Classify this cell by malaria status.
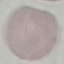

It is uninfected.

Summary:
  - Preparation: thin smear
  - Stain: Giemsa
  - Image type: cell patch, automatically extracted from a larger field of view and resized to 64 × 64 pixels
  - Capture: smartphone through the microscope eyepiece